Name the cell type shown.
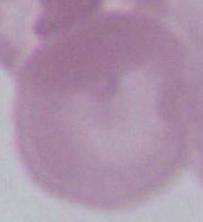

An erythrocyte.

modality: photomicrograph
magnification: 1000x